Point out each Plasmodium parasite.
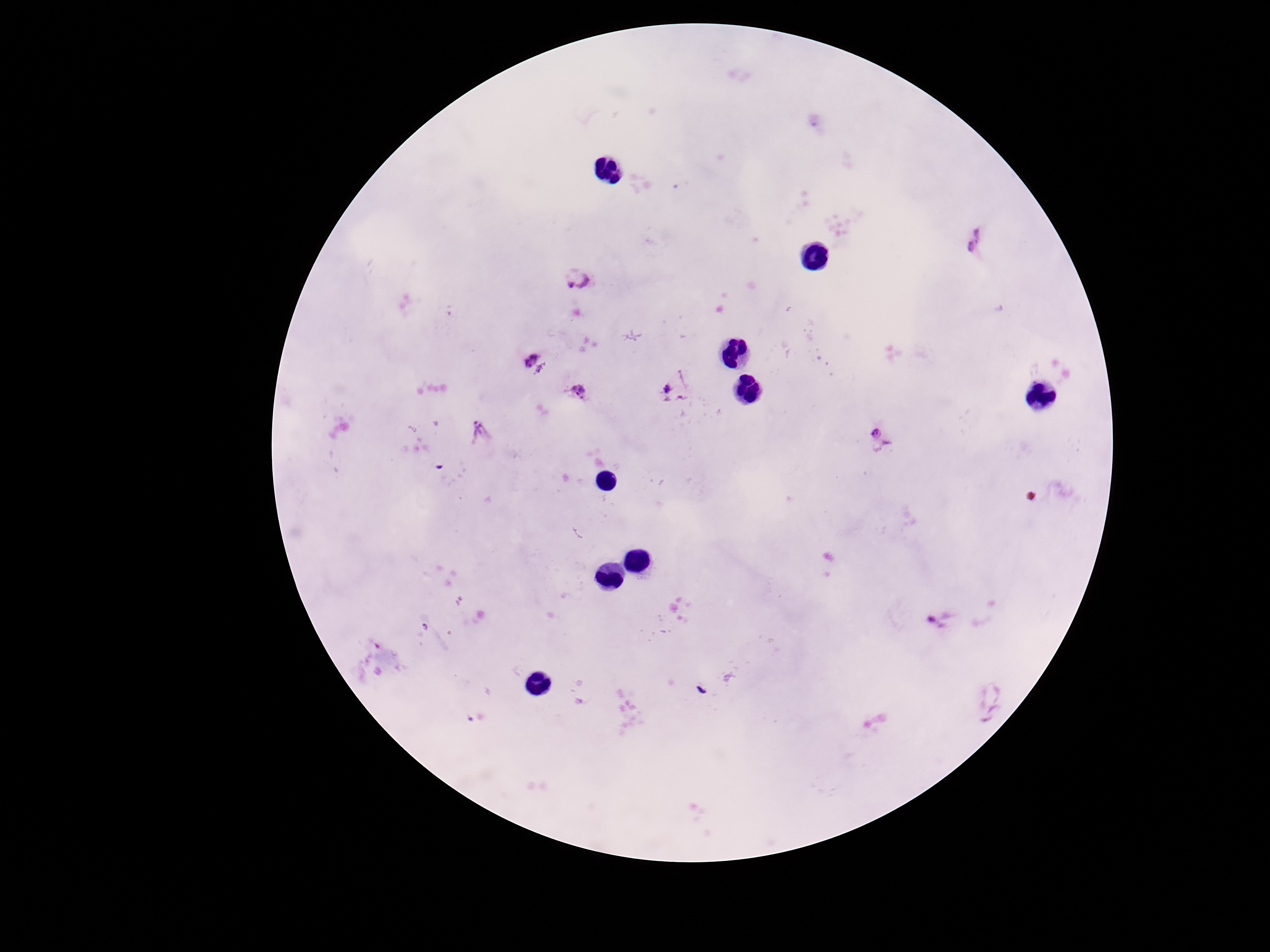

Approximate object centers, in pixels from the top-left corner.
Plasmodium parasites: (x=976, y=239), (x=579, y=279), (x=532, y=360), (x=675, y=386), (x=579, y=391), (x=480, y=430), (x=881, y=440), (x=940, y=620), (x=479, y=719).

{
  "field_of_view": "single",
  "image_size": "1270×952 pixels",
  "patient_malaria_status": "positive",
  "preparation": "thick blood film",
  "magnification": "100x",
  "capture": "smartphone camera through the microscope eyepiece",
  "stain": "Giemsa"
}